Name the parasite shown.
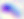
This is Toxoplasma gondii.

{
  "modality": "photomicrograph",
  "magnification": "400x"
}